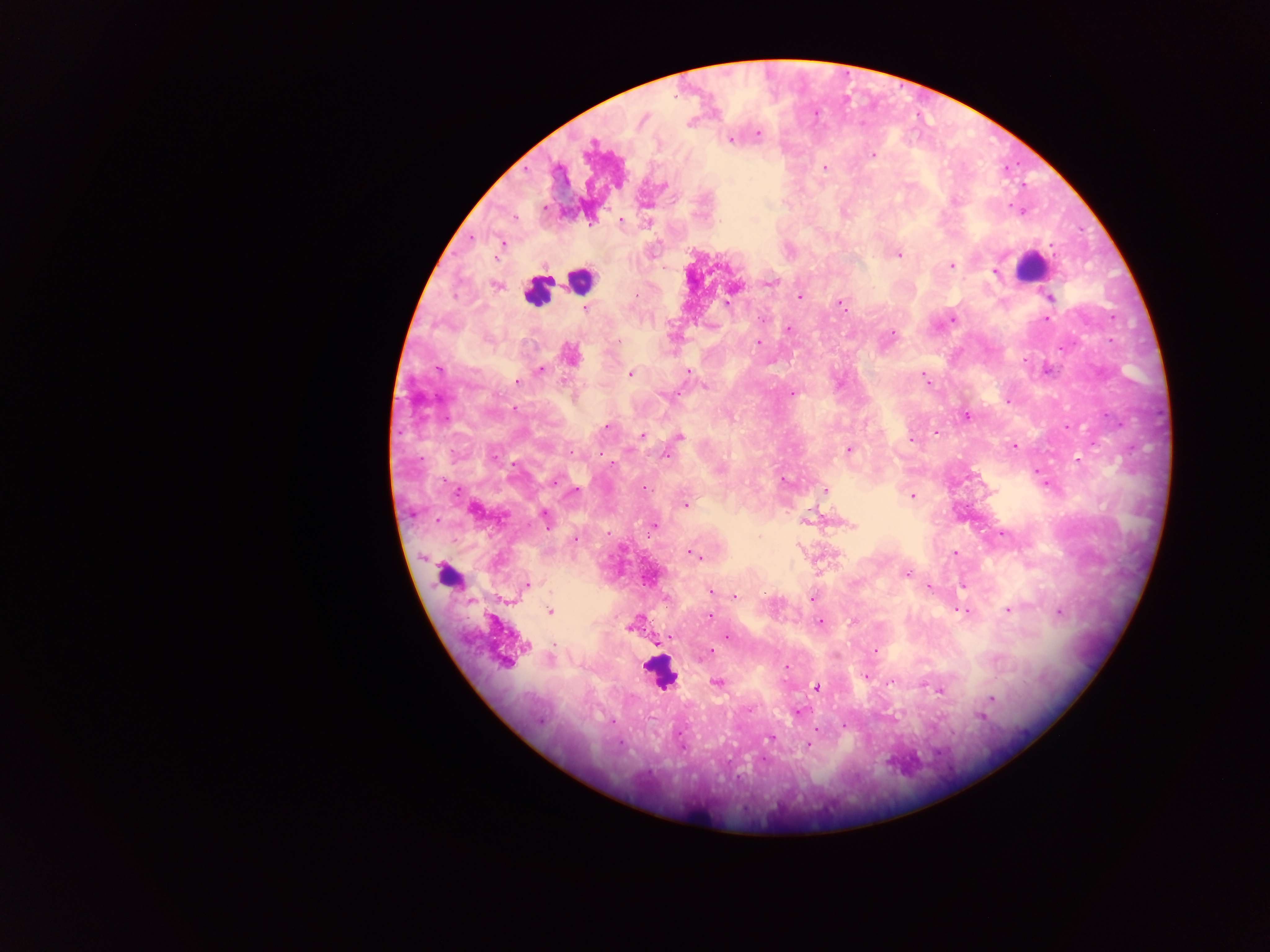
preparation = thick blood film
Plasmodium parasite locations = approximate centers as x y in pixels: 643 119; 758 133; 731 140; 591 144; 872 155; 825 167; 664 184; 543 207; 514 218; 621 220; 648 223; 471 238; 503 243; 898 254; 952 265; 994 271; 771 283; 496 286; 733 289; 799 296; 1050 297; 728 302; 839 303; 585 309; 763 319; 953 319; 1046 319; 788 328; 892 333; 619 342; 759 342; 569 354; 439 370; 540 371; 689 371; 629 374; 923 377; 518 382; 705 386; 792 393; 674 396; 1007 402; 514 409; 966 416; 606 427; 935 433; 642 434; 679 437; 910 440; 1014 446; 848 449; 666 455; 1078 459; 554 481; 783 481; 1047 485; 645 487; 576 490; 825 490; 911 496; 685 505; 545 516; 807 521; 654 525; 852 525; 1003 533; 608 534; 575 540; 955 553; 693 554; 699 558; 906 573; 527 585; 928 587; 711 591; 734 596; 666 597; 812 599; 958 609; 1008 609; 550 611; 964 611; 1060 612; 709 616; 820 621; 853 621; 629 626; 727 636; 670 637; 526 646; 711 651; 875 651; 550 659; 503 663; 786 667; 865 676; 890 682; 717 683; 817 687; 940 690; 992 698; 750 709; 798 712; 980 716; 540 721; 845 725; 679 733; 769 737; 808 744
image size = 1270×952 pixels
country = Ghana
field of view = single
capture = mobile-phone photograph through a microscope
leukocyte locations = approximate centers as x y in pixels: 1031 267; 580 281; 536 292; 448 576; 661 675